Evaluate for Plasmodium parasites.
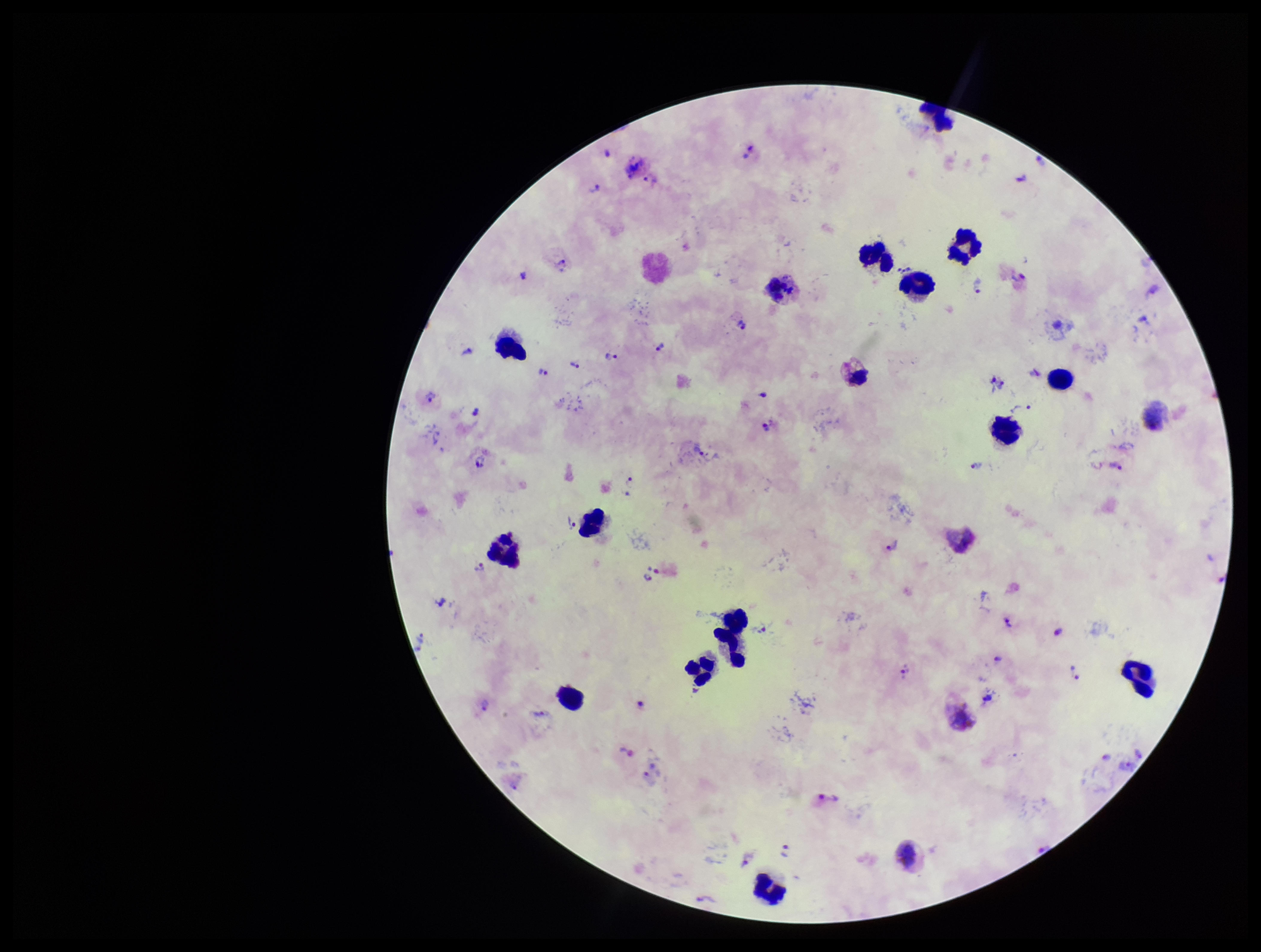
Seen.

preparation = thick blood smear
parasite count = 45
patient malaria status = infected
leukocyte count = 16
image size = 1261×952 pixels
stain = Giemsa
field of view = one from this slide
species reported for this patient = Plasmodium vivax
capture = smartphone photograph through the microscope eyepiece